Report the malaria status of this cell.
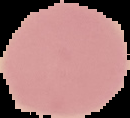

Uninfected.

Summary:
  - Preparation: thin blood smear
  - Image size: 130×118 pixels
  - Image type: cell region segmented out of the field of view; surrounding area masked to black